Assess this cell for malaria.
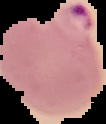
It is parasitized.

{
  "preparation": "thin blood film",
  "image_size": "106×124 pixels",
  "image_type": "segmented cell region with the area outside set to black"
}